Classify this cell by malaria status.
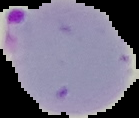
Parasitized.

image_size: 139×118 pixels
preparation: thin blood smear
image_type: segmented cell region with the area outside set to black